Locate Plasmodium parasites and leukocytes.
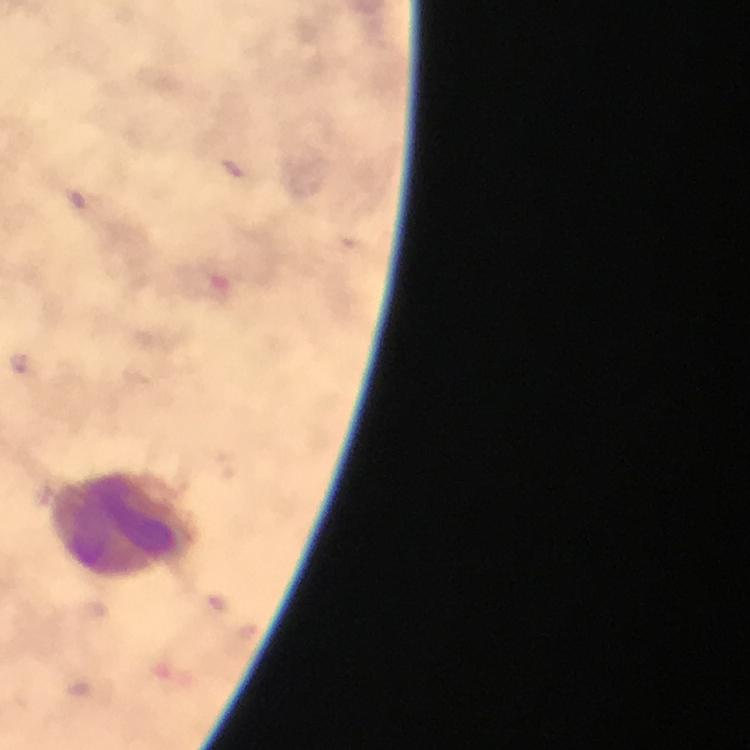
Approximate centers as {x, y} in pixels.
Plasmodium parasites: {232, 167}.
Leukocytes: {123, 524}.

Summary:
  - Cropped from: one field of view
  - Stain: Giemsa
  - Image size: 750×750 pixels
  - Capture: smartphone mounted on the microscope
  - Magnification: 100x
  - Context: from a malaria diagnostic workup
  - Preparation: thick blood smear
  - Immersion oil: used